Report the malaria status of this cell.
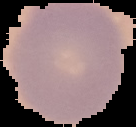
It is uninfected.

Image is 136×127 pixels. Cell region segmented out of the field of view; the surrounding area is masked to black. From a thin blood film.